Comment on the morphology of the erythrocytes.
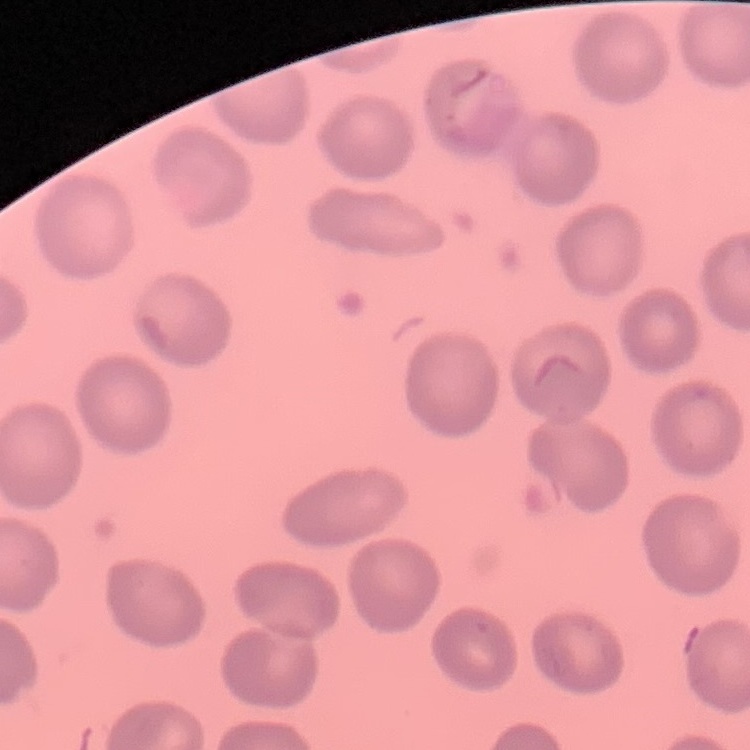
No rouleaux formation.

Summary:
  - Preparation: thin peripheral smear
  - Image type: one tile cut from a larger photomicrograph
  - Stain: Field's or Giemsa